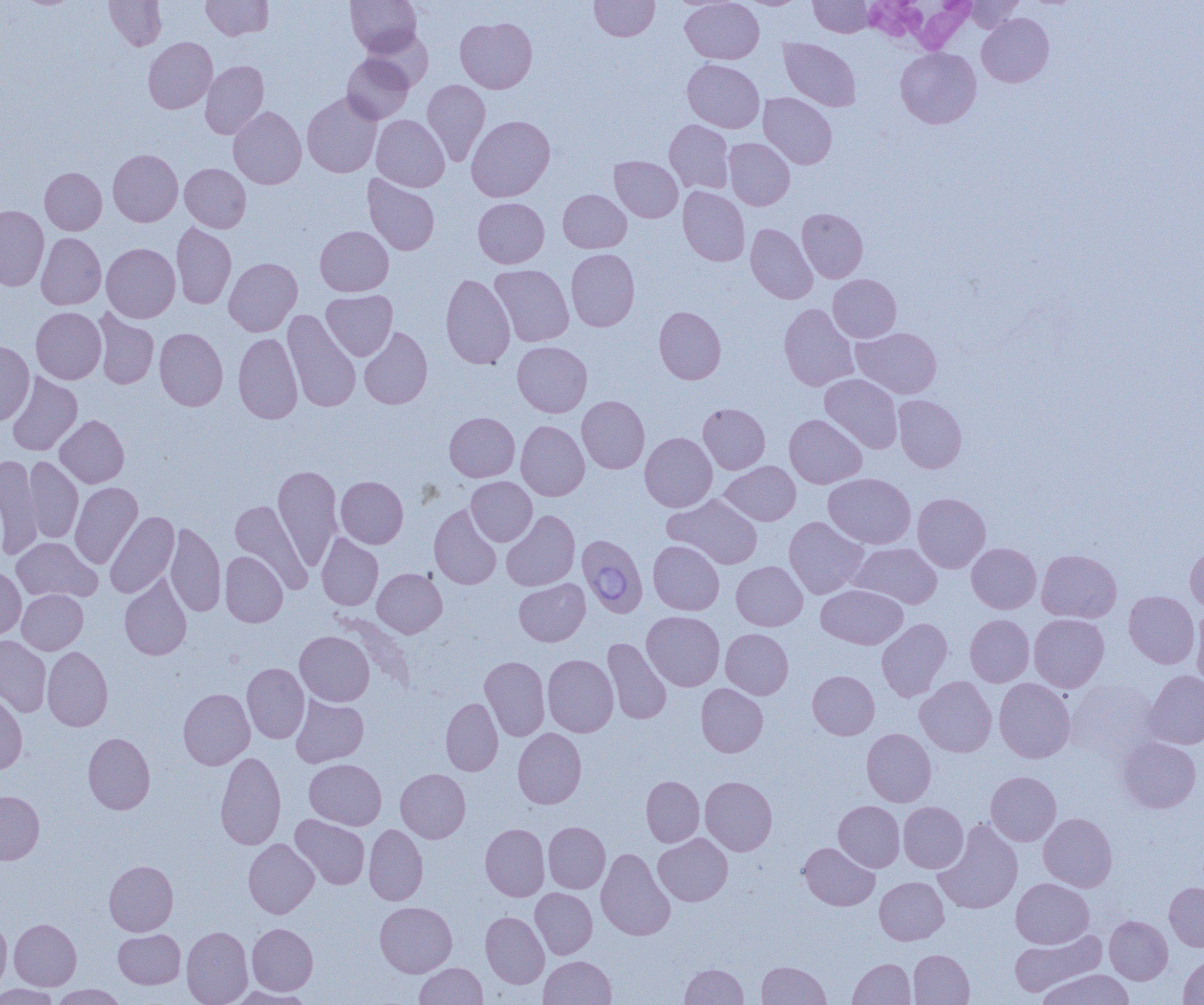

slide-level diagnosis = Babesia divergens
white blood cell locations = approximate bounding boxes as named x1/y1/x2/y2 corners in pixels: (x1=872, y1=3, x2=979, y2=56)
modality = optical microscopy
preparation = thin blood smear
image size = 1204×1005 pixels
uninfected red blood cell locations = approximate bounding boxes as named x1/y1/x2/y2 corners in pixels: (x1=104, y1=0, x2=167, y2=50), (x1=201, y1=0, x2=273, y2=40), (x1=346, y1=0, x2=421, y2=57), (x1=590, y1=0, x2=659, y2=41), (x1=681, y1=0, x2=764, y2=64), (x1=739, y1=0, x2=806, y2=9), (x1=809, y1=0, x2=874, y2=37), (x1=963, y1=0, x2=1026, y2=32), (x1=977, y1=13, x2=1054, y2=87), (x1=455, y1=17, x2=537, y2=93), (x1=362, y1=28, x2=434, y2=89), (x1=143, y1=37, x2=217, y2=113), (x1=779, y1=38, x2=861, y2=112), (x1=895, y1=47, x2=981, y2=128), (x1=342, y1=53, x2=414, y2=124), (x1=682, y1=59, x2=764, y2=133), (x1=200, y1=61, x2=269, y2=139), (x1=422, y1=80, x2=490, y2=166), (x1=302, y1=92, x2=382, y2=178), (x1=758, y1=92, x2=837, y2=169), (x1=228, y1=106, x2=307, y2=189), (x1=371, y1=115, x2=449, y2=192), (x1=466, y1=115, x2=555, y2=201), (x1=664, y1=120, x2=734, y2=194), (x1=724, y1=138, x2=795, y2=210), (x1=108, y1=149, x2=183, y2=226), (x1=610, y1=156, x2=683, y2=222), (x1=180, y1=163, x2=251, y2=232), (x1=40, y1=167, x2=107, y2=235), (x1=363, y1=174, x2=439, y2=256), (x1=678, y1=186, x2=750, y2=266), (x1=558, y1=189, x2=631, y2=253), (x1=473, y1=197, x2=549, y2=268), (x1=0, y1=205, x2=49, y2=290), (x1=797, y1=208, x2=868, y2=283), (x1=171, y1=223, x2=236, y2=309), (x1=746, y1=223, x2=818, y2=303), (x1=315, y1=226, x2=393, y2=296), (x1=36, y1=233, x2=106, y2=309), (x1=101, y1=243, x2=180, y2=322), (x1=566, y1=249, x2=639, y2=331), (x1=224, y1=257, x2=302, y2=336), (x1=489, y1=265, x2=574, y2=346), (x1=440, y1=273, x2=515, y2=369), (x1=828, y1=274, x2=901, y2=342), (x1=321, y1=290, x2=397, y2=360), (x1=779, y1=303, x2=859, y2=391), (x1=654, y1=306, x2=726, y2=384), (x1=31, y1=307, x2=106, y2=384), (x1=93, y1=309, x2=160, y2=389), (x1=283, y1=309, x2=361, y2=412), (x1=359, y1=326, x2=433, y2=409), (x1=852, y1=326, x2=942, y2=399), (x1=154, y1=328, x2=227, y2=410), (x1=233, y1=332, x2=303, y2=424), (x1=0, y1=341, x2=34, y2=425), (x1=512, y1=341, x2=592, y2=417), (x1=7, y1=372, x2=82, y2=455), (x1=820, y1=374, x2=903, y2=453), (x1=577, y1=395, x2=649, y2=473), (x1=893, y1=395, x2=967, y2=473), (x1=698, y1=403, x2=770, y2=474), (x1=445, y1=412, x2=519, y2=482), (x1=784, y1=414, x2=866, y2=488), (x1=55, y1=415, x2=129, y2=488), (x1=516, y1=421, x2=589, y2=501), (x1=640, y1=433, x2=717, y2=512), (x1=0, y1=455, x2=43, y2=559), (x1=24, y1=456, x2=84, y2=543), (x1=721, y1=461, x2=800, y2=525), (x1=273, y1=465, x2=342, y2=570), (x1=823, y1=473, x2=916, y2=548), (x1=336, y1=476, x2=408, y2=548), (x1=466, y1=477, x2=537, y2=546), (x1=70, y1=482, x2=142, y2=568), (x1=912, y1=493, x2=991, y2=573), (x1=663, y1=494, x2=763, y2=569), (x1=230, y1=500, x2=312, y2=591), (x1=429, y1=504, x2=502, y2=589), (x1=501, y1=510, x2=580, y2=591), (x1=105, y1=511, x2=179, y2=599), (x1=784, y1=516, x2=868, y2=599), (x1=165, y1=522, x2=226, y2=616), (x1=317, y1=534, x2=383, y2=610), (x1=11, y1=537, x2=102, y2=602), (x1=648, y1=540, x2=724, y2=614), (x1=849, y1=542, x2=942, y2=608), (x1=966, y1=543, x2=1041, y2=613), (x1=1185, y1=544, x2=1204, y2=613), (x1=1037, y1=549, x2=1121, y2=623), (x1=220, y1=551, x2=287, y2=627), (x1=732, y1=561, x2=807, y2=630), (x1=0, y1=567, x2=26, y2=640), (x1=372, y1=568, x2=447, y2=637), (x1=120, y1=574, x2=192, y2=661), (x1=514, y1=579, x2=590, y2=646), (x1=816, y1=584, x2=908, y2=649), (x1=17, y1=589, x2=87, y2=654), (x1=1124, y1=591, x2=1199, y2=669), (x1=1191, y1=607, x2=1204, y2=689), (x1=642, y1=611, x2=725, y2=691), (x1=1029, y1=614, x2=1109, y2=692), (x1=965, y1=615, x2=1034, y2=687), (x1=876, y1=618, x2=952, y2=701), (x1=721, y1=628, x2=793, y2=699), (x1=295, y1=631, x2=374, y2=706), (x1=0, y1=636, x2=51, y2=717), (x1=603, y1=639, x2=672, y2=724), (x1=42, y1=646, x2=113, y2=731), (x1=542, y1=654, x2=618, y2=737), (x1=480, y1=656, x2=550, y2=740), (x1=242, y1=663, x2=309, y2=743), (x1=808, y1=670, x2=879, y2=739), (x1=1144, y1=670, x2=1204, y2=749), (x1=915, y1=677, x2=997, y2=757), (x1=994, y1=678, x2=1075, y2=763), (x1=1066, y1=678, x2=1162, y2=760), (x1=696, y1=683, x2=768, y2=757), (x1=178, y1=688, x2=255, y2=769), (x1=0, y1=690, x2=27, y2=774), (x1=291, y1=695, x2=369, y2=767), (x1=440, y1=698, x2=503, y2=776), (x1=513, y1=728, x2=587, y2=808), (x1=862, y1=728, x2=936, y2=806), (x1=83, y1=733, x2=155, y2=814), (x1=1117, y1=737, x2=1202, y2=813), (x1=216, y1=751, x2=286, y2=851), (x1=305, y1=759, x2=386, y2=830), (x1=396, y1=768, x2=470, y2=843), (x1=986, y1=771, x2=1061, y2=846), (x1=641, y1=776, x2=704, y2=847), (x1=700, y1=776, x2=777, y2=855), (x1=0, y1=791, x2=44, y2=864), (x1=834, y1=800, x2=905, y2=872), (x1=899, y1=802, x2=968, y2=872), (x1=1038, y1=813, x2=1117, y2=892), (x1=290, y1=814, x2=370, y2=889), (x1=934, y1=820, x2=1023, y2=914), (x1=543, y1=822, x2=610, y2=893), (x1=364, y1=824, x2=428, y2=905), (x1=480, y1=824, x2=550, y2=901), (x1=654, y1=833, x2=733, y2=906), (x1=243, y1=839, x2=319, y2=918), (x1=799, y1=842, x2=879, y2=910), (x1=596, y1=848, x2=675, y2=940), (x1=104, y1=860, x2=178, y2=936), (x1=875, y1=877, x2=949, y2=944), (x1=1011, y1=878, x2=1093, y2=948), (x1=1164, y1=882, x2=1204, y2=951), (x1=530, y1=888, x2=597, y2=959), (x1=375, y1=902, x2=457, y2=977), (x1=480, y1=911, x2=549, y2=988), (x1=1105, y1=915, x2=1172, y2=984), (x1=0, y1=918, x2=11, y2=995), (x1=10, y1=918, x2=81, y2=990), (x1=247, y1=923, x2=318, y2=995), (x1=182, y1=926, x2=253, y2=1005), (x1=113, y1=929, x2=185, y2=988), (x1=1009, y1=930, x2=1105, y2=997), (x1=909, y1=949, x2=974, y2=1005), (x1=1179, y1=955, x2=1204, y2=1004), (x1=539, y1=956, x2=616, y2=1005), (x1=848, y1=958, x2=915, y2=1005), (x1=757, y1=961, x2=830, y2=1004), (x1=415, y1=962, x2=487, y2=1004), (x1=680, y1=964, x2=748, y2=1004), (x1=1035, y1=969, x2=1135, y2=1005), (x1=0, y1=984, x2=60, y2=1005), (x1=50, y1=984, x2=127, y2=1004), (x1=226, y1=986, x2=317, y2=1004)
field of view = one of a larger specimen
magnification = 1000x
Babesia divergens-infected red blood cell locations = approximate bounding boxes as named x1/y1/x2/y2 corners in pixels: (x1=579, y1=537, x2=645, y2=616)